Name the parasite shown.
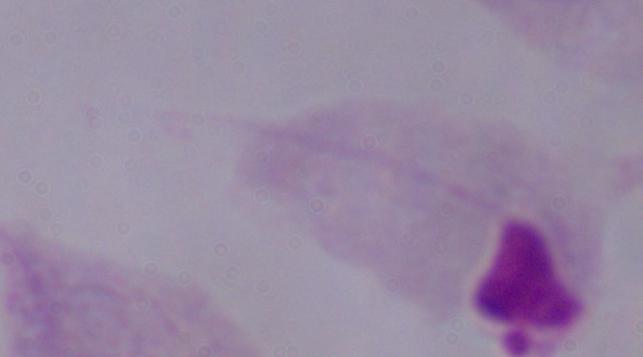

This is a trichomonad.

1000x magnification. Micrograph.